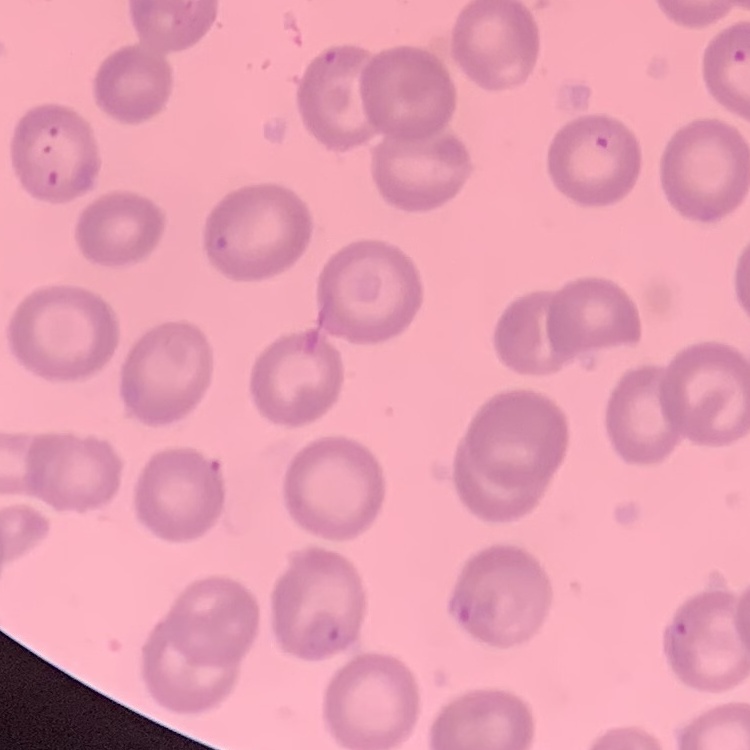

erythrocyte morphology = no rouleaux formation
image type = square crop of a larger photomicrograph
stain = Field's or Giemsa
preparation = thin peripheral smear